Locate every blood parasite and identify its species.
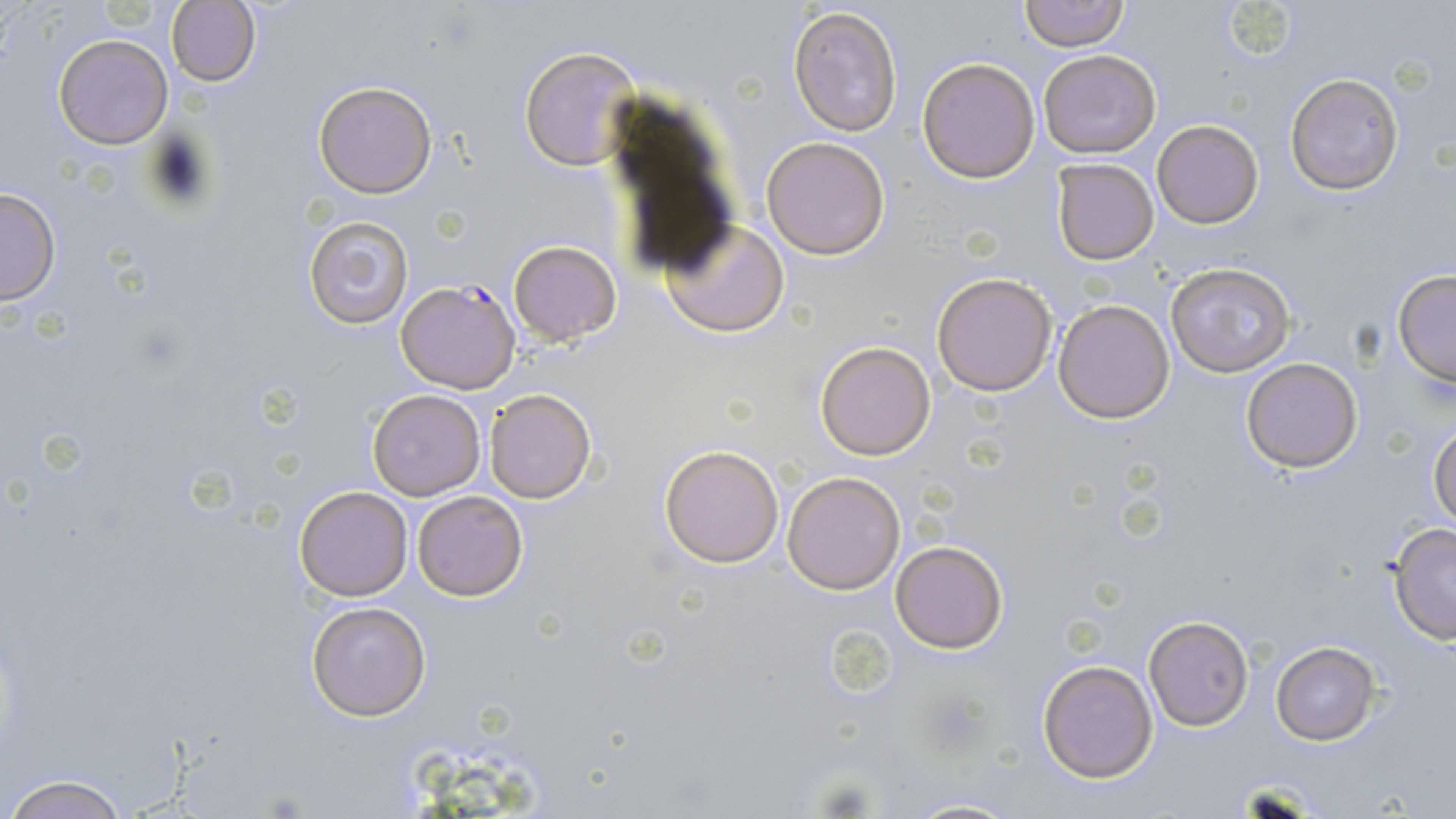
Approximate bounding boxes as named x1/y1/x2/y2 corners in pixels.
Plasmodium falciparum-infected red blood cells: (x1=397, y1=279, x2=519, y2=393).
No Plasmodium ovale, Plasmodium malariae, Plasmodium vivax, Babesia divergens, or Trypanosoma brucei observed.

Uninfected red blood cell locations: (x1=1018, y1=0, x2=1128, y2=50), (x1=167, y1=1, x2=261, y2=87), (x1=1220, y1=1, x2=1302, y2=69), (x1=787, y1=3, x2=904, y2=139), (x1=53, y1=33, x2=173, y2=150), (x1=519, y1=45, x2=642, y2=171), (x1=1038, y1=50, x2=1160, y2=158), (x1=916, y1=56, x2=1040, y2=183), (x1=1284, y1=72, x2=1404, y2=195), (x1=312, y1=79, x2=437, y2=198), (x1=1151, y1=120, x2=1263, y2=229), (x1=760, y1=135, x2=892, y2=260), (x1=1052, y1=158, x2=1159, y2=264), (x1=0, y1=187, x2=61, y2=307), (x1=303, y1=215, x2=413, y2=329), (x1=660, y1=218, x2=790, y2=338), (x1=509, y1=240, x2=623, y2=347), (x1=1164, y1=262, x2=1296, y2=379), (x1=1391, y1=270, x2=1456, y2=388), (x1=931, y1=271, x2=1057, y2=395), (x1=1053, y1=299, x2=1176, y2=423), (x1=814, y1=341, x2=936, y2=460), (x1=1239, y1=356, x2=1365, y2=474), (x1=483, y1=388, x2=597, y2=504), (x1=368, y1=389, x2=486, y2=501), (x1=1430, y1=423, x2=1456, y2=529), (x1=659, y1=444, x2=784, y2=566), (x1=782, y1=472, x2=906, y2=593), (x1=296, y1=485, x2=413, y2=599), (x1=411, y1=490, x2=528, y2=602), (x1=1386, y1=523, x2=1456, y2=645), (x1=889, y1=539, x2=1011, y2=655), (x1=306, y1=600, x2=432, y2=721), (x1=1142, y1=614, x2=1253, y2=732), (x1=1271, y1=643, x2=1380, y2=745), (x1=1037, y1=659, x2=1158, y2=784), (x1=5, y1=773, x2=131, y2=819), (x1=895, y1=796, x2=1020, y2=818). Slide-level diagnosis: Plasmodium falciparum. Optical microscopy. May-Grünwald-Giemsa stain. Thin blood film. Image is 1456×819 pixels. Single field of view. Captured at 1000x magnification.